Locate and identify every blood parasite.
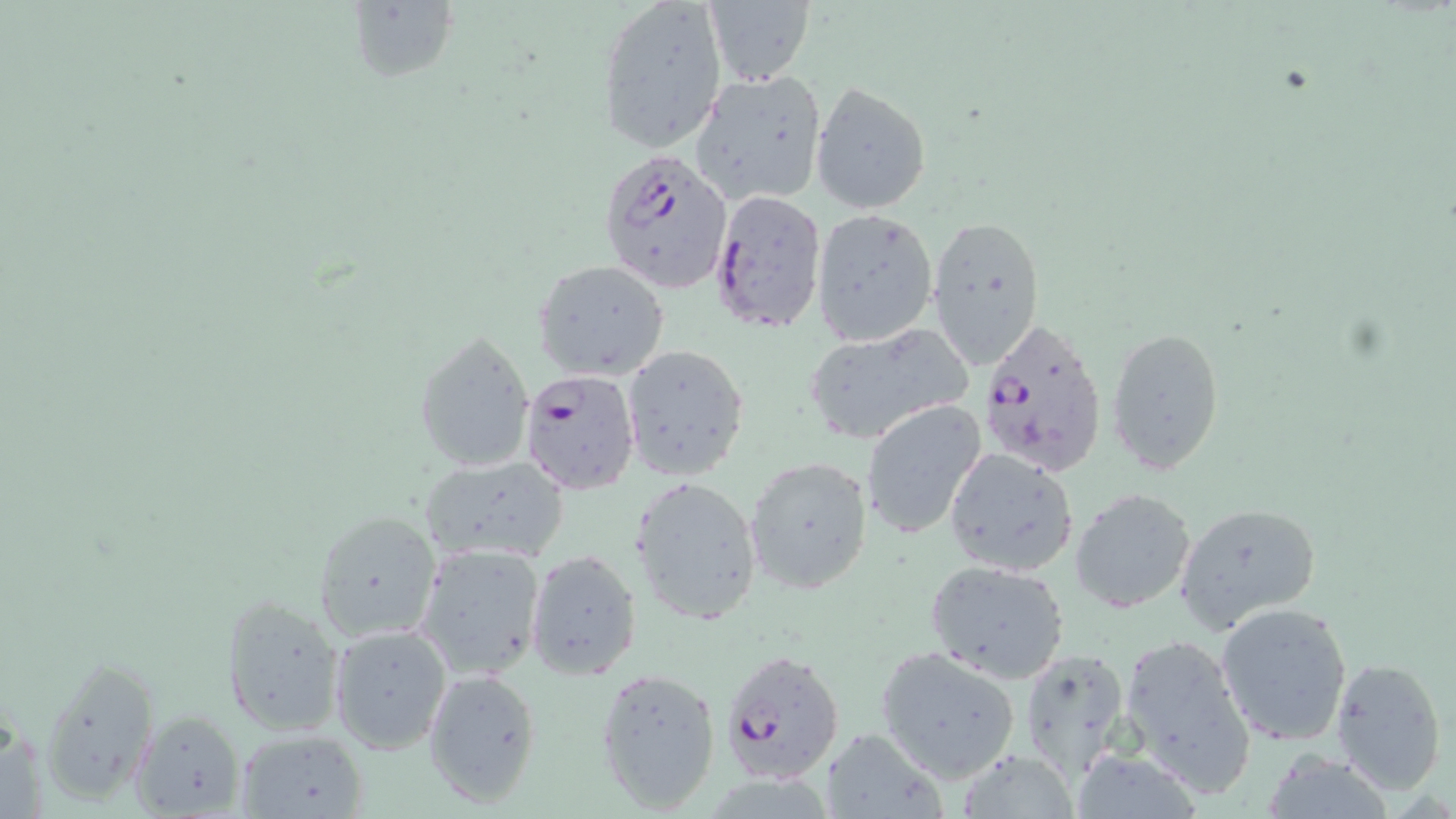

Approximate bounding boxes as (x1, y1, x2, y2) in pixels.
Plasmodium falciparum-infected red blood cells: (596, 147, 732, 291), (708, 190, 826, 335), (976, 314, 1110, 481), (518, 366, 640, 496), (719, 647, 847, 786).
No Plasmodium ovale, Plasmodium malariae, Plasmodium vivax, Babesia divergens, or Trypanosoma brucei observed.

Uninfected red blood cell locations: (347, 1, 458, 87), (596, 1, 725, 151), (699, 3, 814, 86), (689, 70, 826, 207), (809, 80, 932, 215), (812, 208, 939, 347), (926, 212, 1047, 372), (534, 260, 669, 381), (801, 324, 972, 447), (1106, 324, 1226, 474), (415, 330, 535, 474), (620, 343, 749, 481), (860, 399, 987, 543), (944, 447, 1078, 577), (420, 455, 569, 563), (745, 455, 873, 595), (631, 475, 763, 626), (1070, 488, 1197, 613), (1174, 504, 1320, 630), (314, 510, 442, 643), (415, 542, 546, 681), (525, 549, 643, 682), (925, 558, 1072, 683), (222, 594, 346, 737), (1214, 601, 1354, 746), (329, 624, 451, 753), (1116, 634, 1255, 801), (875, 646, 1023, 784), (1019, 648, 1135, 789), (37, 653, 160, 804), (1330, 656, 1448, 795), (594, 667, 720, 813), (423, 670, 543, 807), (128, 709, 246, 818), (819, 727, 947, 818), (232, 728, 371, 819), (950, 747, 1084, 819), (1262, 751, 1392, 817). Slide-level diagnosis: Plasmodium falciparum. One field of a larger specimen. Thin blood film. Optical microscopy. Image is 1456×819 pixels. May-Grünwald-Giemsa-stained preparation. Captured at 1000x magnification.